Name the blood parasite species.
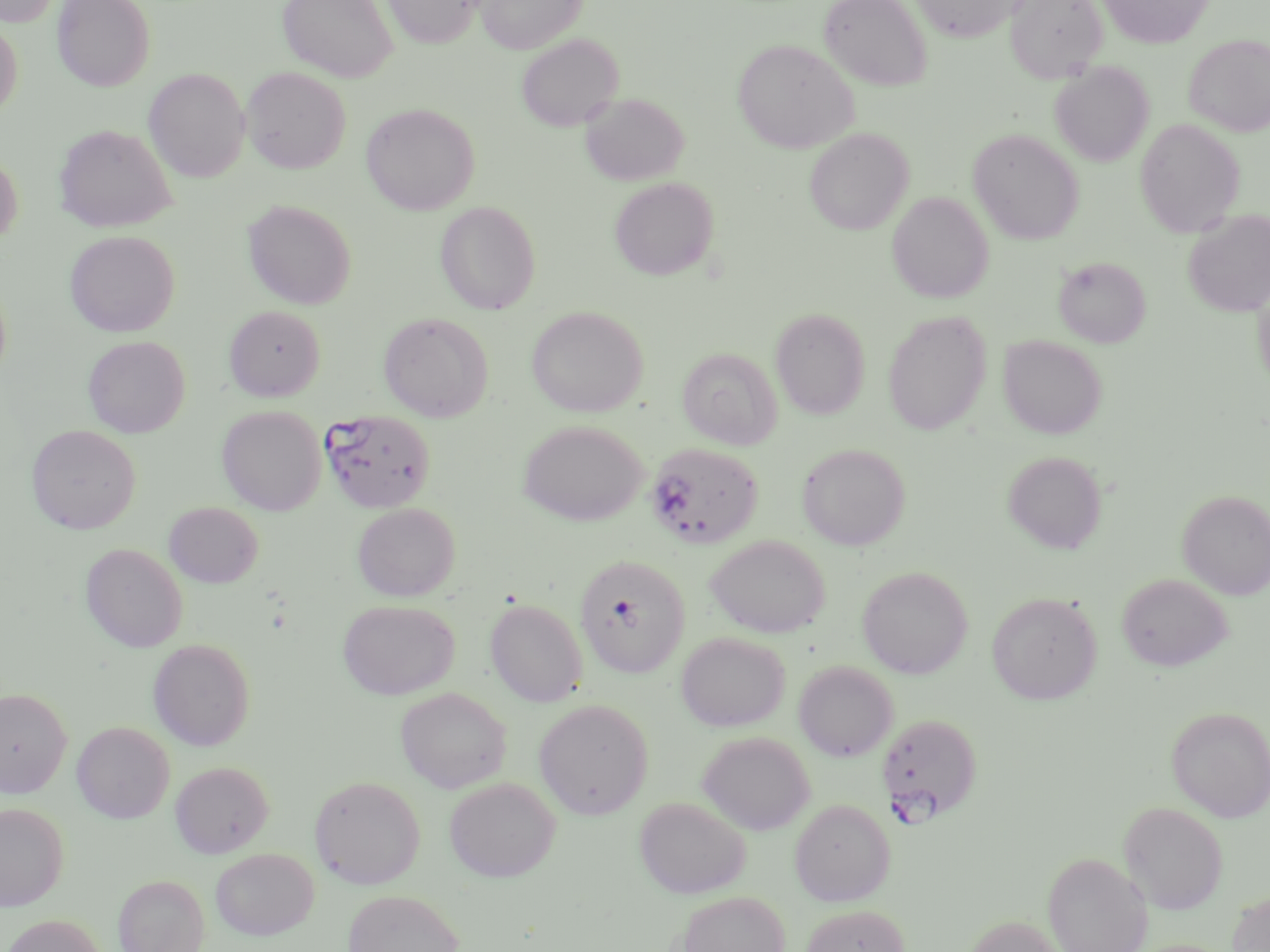

Plasmodium falciparum.

Approximate bounding boxes as named x1/y1/x2/y2 corners in pixels. Uninfected red blood cell locations: (x1=1, y1=0, x2=61, y2=27), (x1=53, y1=0, x2=155, y2=91), (x1=278, y1=0, x2=397, y2=82), (x1=383, y1=0, x2=484, y2=48), (x1=476, y1=0, x2=585, y2=53), (x1=819, y1=0, x2=932, y2=91), (x1=910, y1=0, x2=1024, y2=42), (x1=1005, y1=0, x2=1108, y2=83), (x1=1097, y1=0, x2=1213, y2=49), (x1=0, y1=19, x2=23, y2=120), (x1=516, y1=33, x2=623, y2=132), (x1=1184, y1=34, x2=1270, y2=136), (x1=733, y1=39, x2=858, y2=153), (x1=1050, y1=62, x2=1154, y2=166), (x1=241, y1=67, x2=351, y2=174), (x1=144, y1=68, x2=250, y2=183), (x1=580, y1=92, x2=689, y2=186), (x1=361, y1=102, x2=480, y2=215), (x1=1135, y1=118, x2=1245, y2=238), (x1=54, y1=123, x2=177, y2=232), (x1=804, y1=128, x2=913, y2=235), (x1=968, y1=128, x2=1084, y2=245), (x1=0, y1=153, x2=23, y2=246), (x1=610, y1=177, x2=719, y2=280), (x1=887, y1=191, x2=994, y2=304), (x1=242, y1=199, x2=357, y2=309), (x1=435, y1=200, x2=541, y2=314), (x1=1183, y1=208, x2=1270, y2=317), (x1=64, y1=230, x2=180, y2=337), (x1=1054, y1=256, x2=1151, y2=347), (x1=1252, y1=277, x2=1270, y2=398), (x1=0, y1=282, x2=11, y2=386), (x1=224, y1=305, x2=325, y2=401), (x1=527, y1=306, x2=648, y2=417), (x1=770, y1=308, x2=870, y2=419), (x1=883, y1=311, x2=991, y2=435), (x1=378, y1=312, x2=494, y2=422), (x1=999, y1=334, x2=1107, y2=439), (x1=83, y1=335, x2=190, y2=438), (x1=677, y1=347, x2=782, y2=450), (x1=217, y1=406, x2=326, y2=516), (x1=518, y1=420, x2=649, y2=526), (x1=26, y1=424, x2=141, y2=534), (x1=797, y1=443, x2=911, y2=550), (x1=1002, y1=451, x2=1107, y2=554), (x1=1178, y1=489, x2=1270, y2=599), (x1=164, y1=501, x2=263, y2=588), (x1=352, y1=503, x2=460, y2=601), (x1=706, y1=535, x2=830, y2=638), (x1=81, y1=543, x2=187, y2=652), (x1=574, y1=553, x2=691, y2=678), (x1=858, y1=566, x2=973, y2=678), (x1=1117, y1=573, x2=1233, y2=671), (x1=987, y1=592, x2=1101, y2=704), (x1=485, y1=598, x2=588, y2=707), (x1=338, y1=599, x2=460, y2=700), (x1=676, y1=631, x2=790, y2=732), (x1=148, y1=639, x2=255, y2=750), (x1=793, y1=660, x2=898, y2=761), (x1=0, y1=687, x2=71, y2=797), (x1=396, y1=687, x2=511, y2=793), (x1=534, y1=698, x2=654, y2=819), (x1=1166, y1=706, x2=1270, y2=821), (x1=72, y1=721, x2=175, y2=823), (x1=698, y1=731, x2=815, y2=835), (x1=171, y1=761, x2=273, y2=857), (x1=309, y1=774, x2=425, y2=889), (x1=444, y1=777, x2=561, y2=882), (x1=635, y1=796, x2=750, y2=898), (x1=789, y1=798, x2=895, y2=906), (x1=1119, y1=801, x2=1228, y2=914), (x1=0, y1=802, x2=68, y2=910), (x1=210, y1=847, x2=319, y2=939), (x1=1042, y1=852, x2=1152, y2=952), (x1=113, y1=874, x2=210, y2=952), (x1=344, y1=889, x2=464, y2=952), (x1=1226, y1=890, x2=1270, y2=952), (x1=677, y1=891, x2=790, y2=952), (x1=800, y1=904, x2=910, y2=952), (x1=964, y1=914, x2=1068, y2=952), (x1=0, y1=915, x2=107, y2=952). Plasmodium falciparum-infected red blood cell locations: (x1=321, y1=409, x2=436, y2=513), (x1=646, y1=442, x2=764, y2=549), (x1=877, y1=712, x2=983, y2=822). Single field of view. Light microscopy. Thin blood film. 1000x magnification. Image is 1270×952 pixels. May-Grünwald-Giemsa stain.